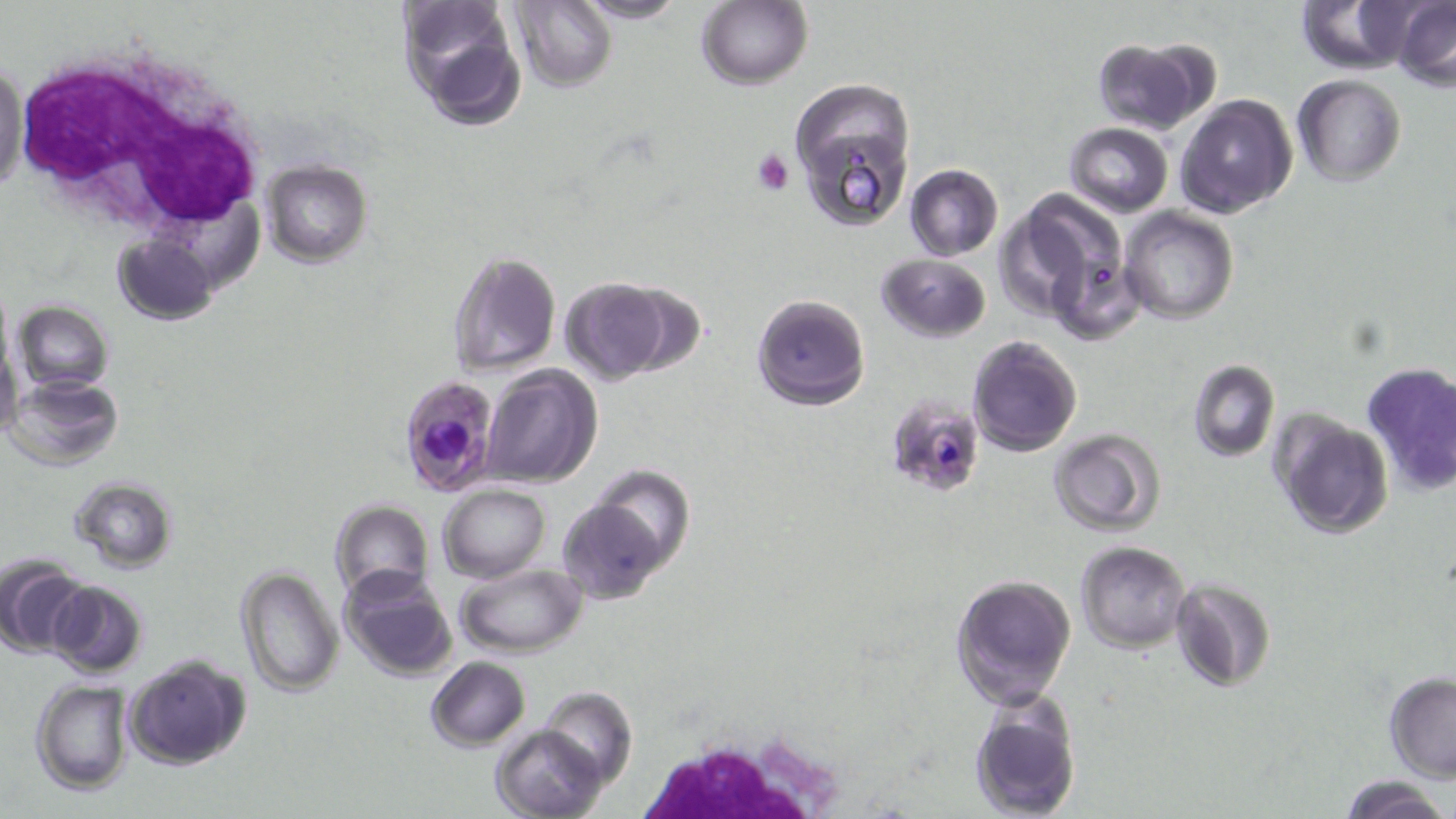 Approximate bounding boxes as named x1/y1/x2/y2 corners in pixels. Platelet locations: (x1=751, y1=148, x2=794, y2=194). Plasmodium falciparum-infected red blood cell locations: (x1=395, y1=378, x2=502, y2=495), (x1=885, y1=395, x2=986, y2=496). White blood cell locations: (x1=11, y1=44, x2=268, y2=242), (x1=637, y1=737, x2=854, y2=816). Uninfected red blood cell locations: (x1=397, y1=0, x2=526, y2=128), (x1=574, y1=0, x2=688, y2=24), (x1=1296, y1=0, x2=1420, y2=73), (x1=508, y1=1, x2=616, y2=90), (x1=698, y1=1, x2=812, y2=90), (x1=1392, y1=2, x2=1456, y2=90), (x1=1090, y1=37, x2=1209, y2=133), (x1=0, y1=59, x2=26, y2=201), (x1=1293, y1=76, x2=1406, y2=188), (x1=791, y1=84, x2=914, y2=234), (x1=1174, y1=94, x2=1296, y2=218), (x1=1065, y1=122, x2=1173, y2=216), (x1=261, y1=161, x2=373, y2=267), (x1=903, y1=165, x2=1003, y2=260), (x1=1003, y1=189, x2=1130, y2=324), (x1=1120, y1=207, x2=1239, y2=325), (x1=113, y1=233, x2=217, y2=328), (x1=446, y1=248, x2=561, y2=376), (x1=876, y1=253, x2=990, y2=342), (x1=561, y1=279, x2=674, y2=382), (x1=751, y1=292, x2=870, y2=409), (x1=13, y1=302, x2=114, y2=392), (x1=1, y1=330, x2=22, y2=442), (x1=967, y1=334, x2=1084, y2=456), (x1=1188, y1=359, x2=1279, y2=463), (x1=1361, y1=362, x2=1456, y2=495), (x1=479, y1=366, x2=602, y2=488), (x1=7, y1=376, x2=123, y2=470), (x1=1273, y1=412, x2=1394, y2=538), (x1=1048, y1=429, x2=1165, y2=535), (x1=590, y1=467, x2=696, y2=574), (x1=69, y1=475, x2=178, y2=574), (x1=439, y1=483, x2=549, y2=583), (x1=559, y1=493, x2=673, y2=604), (x1=330, y1=500, x2=433, y2=603), (x1=1076, y1=540, x2=1190, y2=653), (x1=3, y1=558, x2=89, y2=658), (x1=456, y1=563, x2=586, y2=656), (x1=235, y1=565, x2=342, y2=698), (x1=337, y1=566, x2=458, y2=683), (x1=949, y1=572, x2=1076, y2=711), (x1=1169, y1=577, x2=1274, y2=692), (x1=47, y1=581, x2=149, y2=678), (x1=124, y1=655, x2=252, y2=771), (x1=425, y1=657, x2=530, y2=751), (x1=1384, y1=673, x2=1456, y2=782), (x1=30, y1=680, x2=135, y2=795), (x1=539, y1=685, x2=638, y2=788), (x1=968, y1=696, x2=1081, y2=819), (x1=490, y1=723, x2=608, y2=819), (x1=1339, y1=778, x2=1454, y2=819). Slide-level diagnosis: Plasmodium falciparum. May-Grünwald-Giemsa stain. 1000x magnification. One field of a larger specimen. Thin blood smear. Image is 1456×819 pixels. Optical microscopy.